Name the parasite shown.
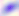

This is Toxoplasma gondii.

400x magnification. Photomicrograph.